Assess the morphology of the erythrocytes.
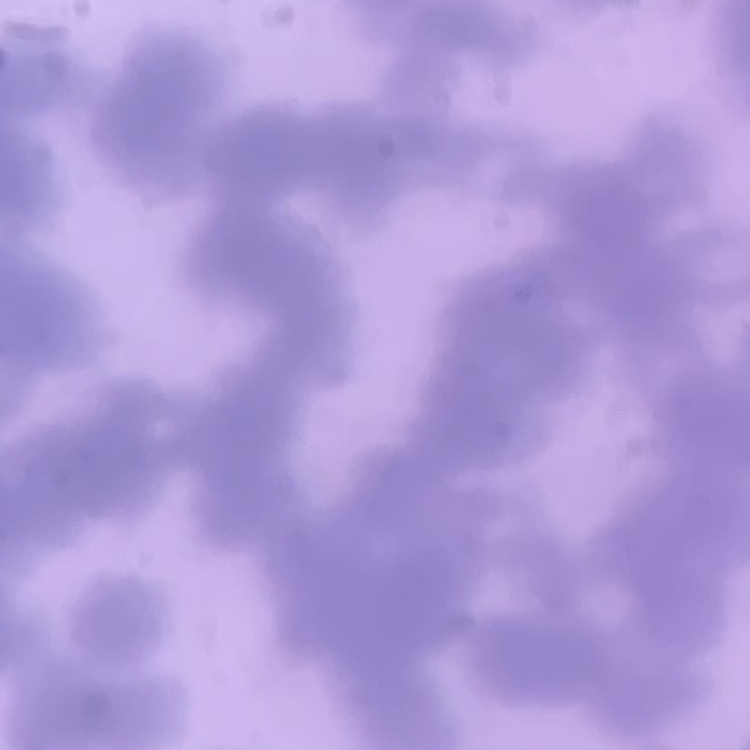

They show rouleaux formation.

Summary:
  - Stain: Field's or Giemsa
  - Preparation: thin blood smear
  - Image type: square crop of a larger photomicrograph